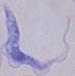
Summary:
  - Modality: micrograph
  - Magnification: 1000x
  - Identification: trypanosome